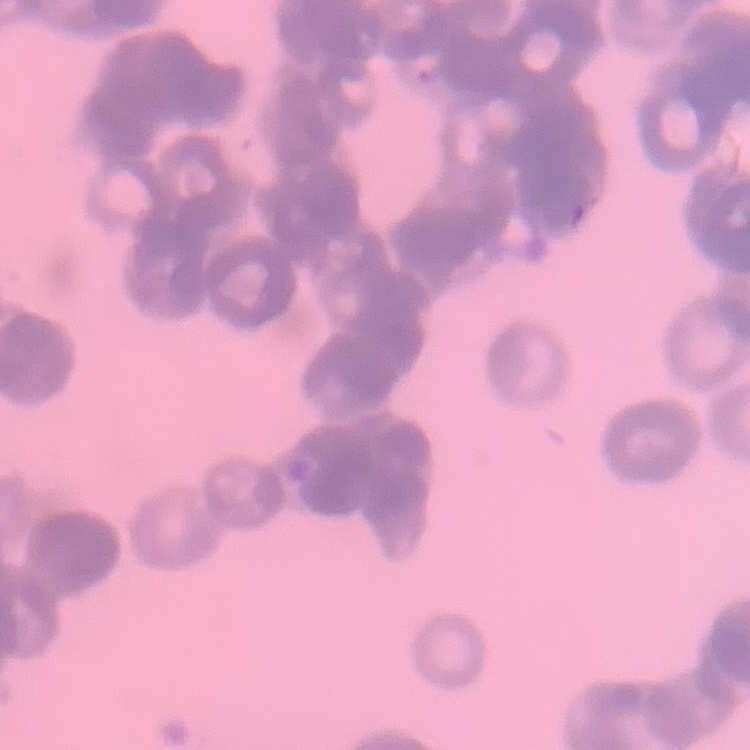

The erythrocytes show rouleaux formation. Stained with either Field's or Giemsa. Square crop of a larger photomicrograph. Thin blood film.